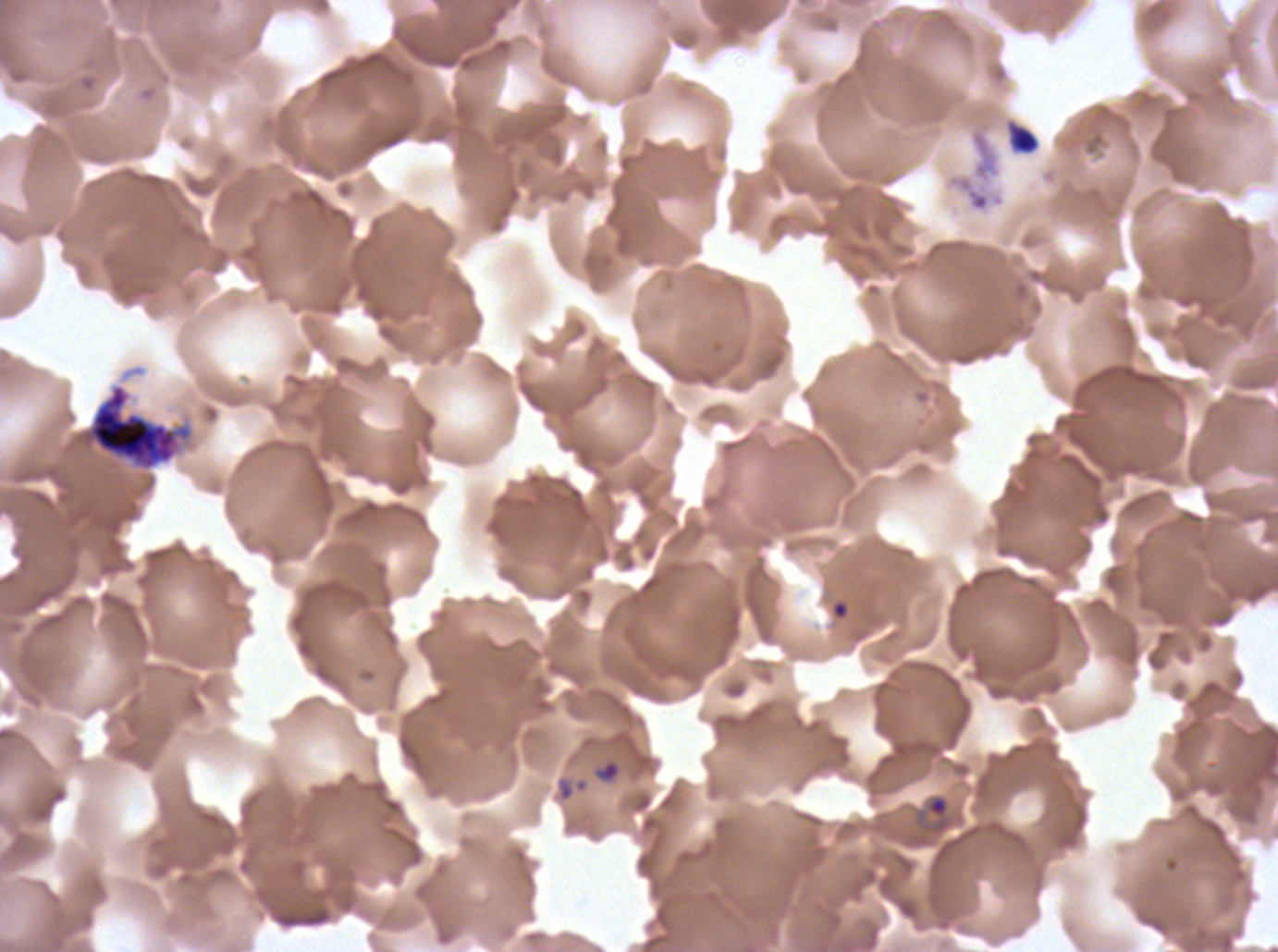

Approximate bounding rectangles given as corner coordinates in pixels from the top-left. Debris locations: (x1=1009, y1=126, x2=1039, y2=154). Ring locations: (x1=593, y1=759, x2=621, y2=784), (x1=914, y1=793, x2=952, y2=835). Early schizont locations: (x1=83, y1=384, x2=191, y2=470). One sub-image of a larger composite. Image is 1278×952 pixels. Thin blood film. Plasmodium falciparum cultured ex vivo for 24 to 48 hours, from a patient in The Gambia. Life-cycle stages observed: ring, early schizont. Giemsa stain.